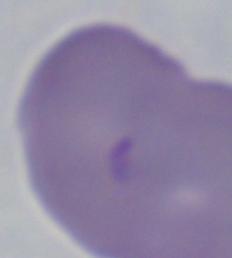
{
  "identification": "Babesia",
  "magnification": "1000x",
  "modality": "micrograph"
}